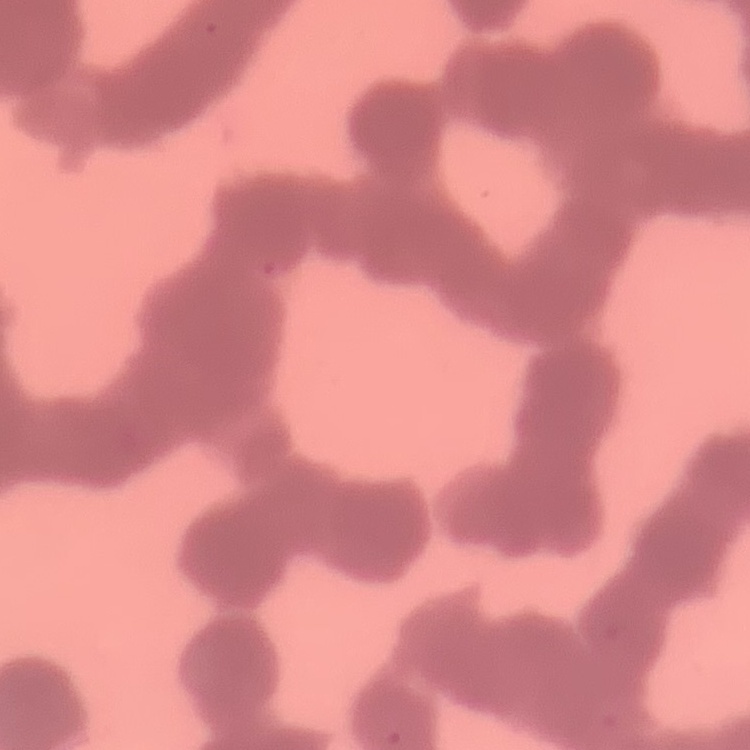

The red blood cells show rouleaux formation. Square crop of a larger photomicrograph. Thin blood film. Stained with either Field's or Giemsa.